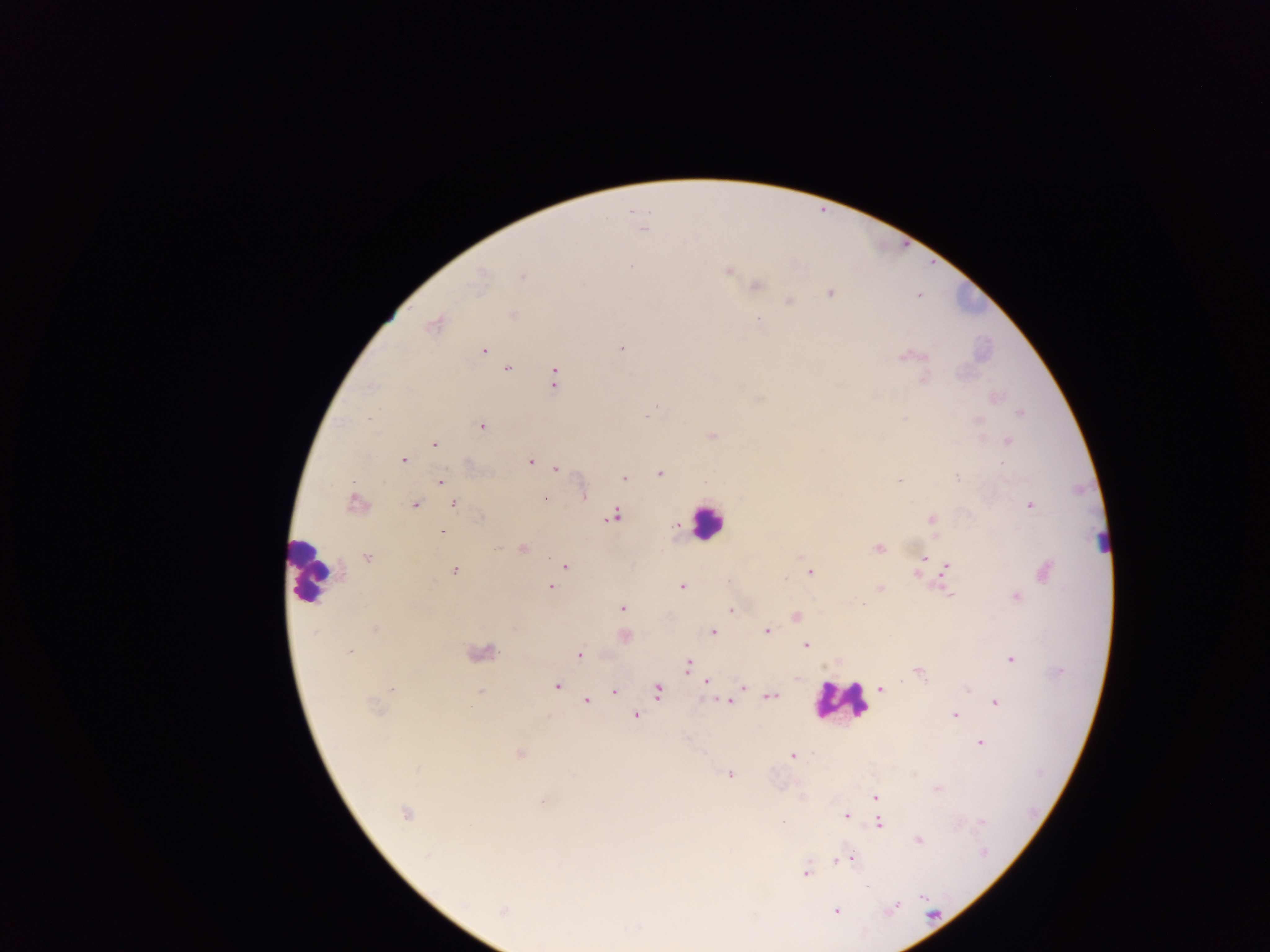

Approximate centers as [x, y] in pixels. Leukocyte locations: [707, 521], [1101, 539], [310, 570], [840, 700]. Plasmodium parasite locations: [643, 228], [631, 267], [728, 271], [523, 276], [479, 277], [756, 286], [830, 293], [789, 302], [512, 315], [758, 320], [433, 325], [621, 348], [484, 350], [902, 356], [921, 356], [508, 368], [555, 378], [924, 379], [656, 407], [1020, 413], [368, 419], [978, 421], [482, 426], [712, 437], [1008, 441], [434, 444], [403, 460], [530, 461], [1002, 462], [556, 468], [660, 473], [624, 478], [957, 478], [441, 481], [900, 481], [584, 495], [546, 500], [356, 502], [454, 504], [416, 505], [1030, 505], [613, 516], [931, 519], [442, 532], [499, 547], [878, 548], [523, 549], [368, 557], [925, 558], [565, 565], [947, 566], [454, 571], [1046, 571], [810, 572], [916, 574], [682, 586], [551, 587], [881, 588], [950, 594], [1017, 597], [863, 604], [621, 608], [731, 611], [796, 617], [375, 628], [767, 631], [713, 632], [315, 633], [625, 636], [806, 644], [350, 651], [483, 653], [579, 655], [1011, 659], [687, 665], [919, 674], [706, 682], [557, 686], [742, 687], [881, 688], [392, 689], [967, 689], [657, 690], [480, 691], [614, 691], [771, 696], [587, 701], [730, 702], [996, 702], [375, 708], [637, 715], [955, 716], [980, 743], [520, 754], [791, 755], [729, 775], [936, 788], [875, 797], [541, 802], [405, 814], [845, 816], [981, 821], [783, 822], [880, 824], [919, 840], [426, 857], [839, 860], [851, 860], [806, 873], [894, 907], [503, 911], [836, 911]. Single field of view. Image is 1270×952 pixels. Thick blood film. Sample from Ghana. Photographed through a microscope with a mobile-phone camera.